Give a bounding box for every malaria parasite, every leukocyte, and every artifact (stain precipitate or debris).
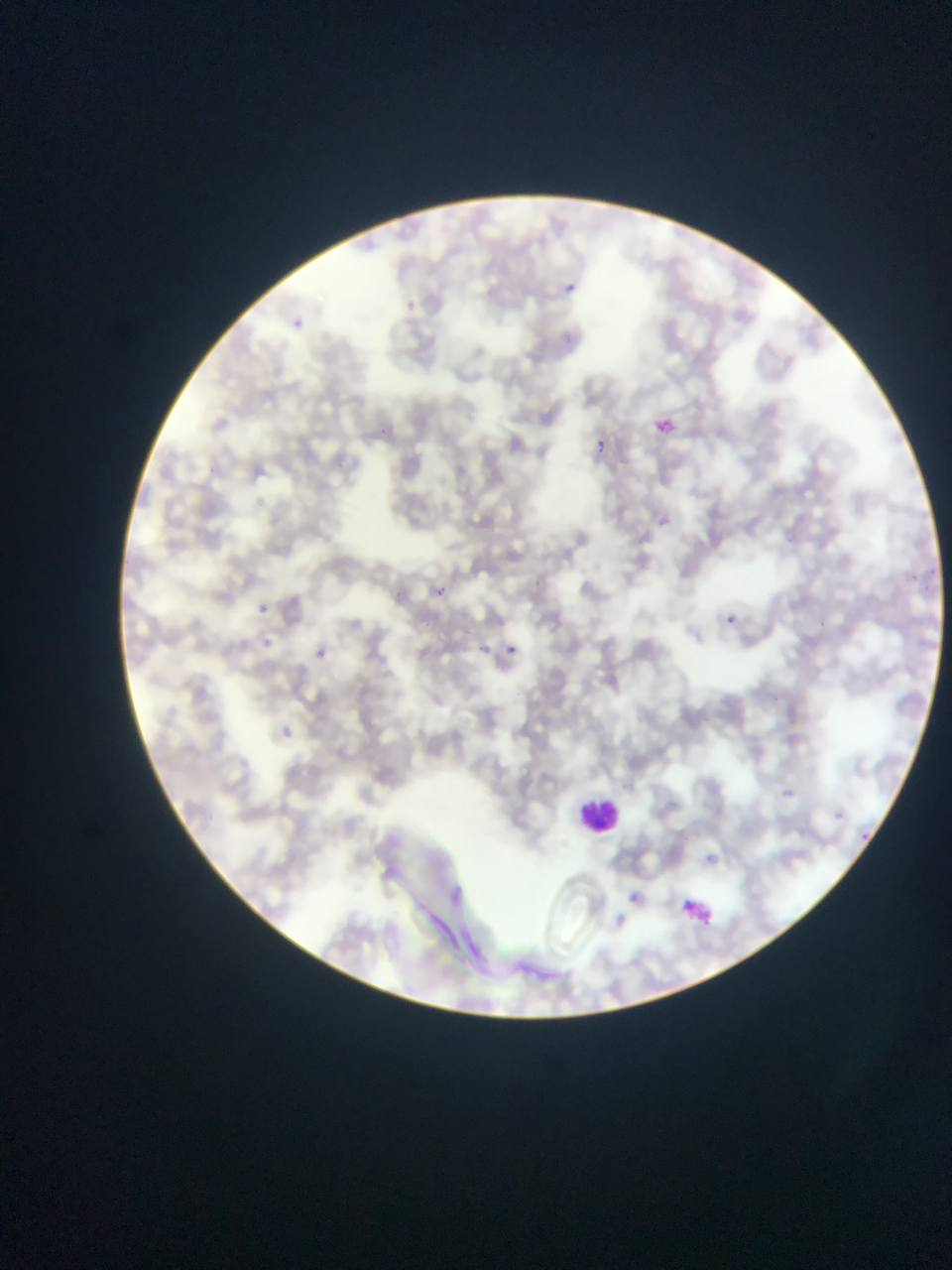

Approximate bounding boxes as {left, top, right, bottom} in pixels.
Malaria parasites: {560, 278, 581, 298}, {402, 279, 435, 317}, {296, 313, 336, 348}, {653, 412, 684, 443}, {598, 435, 629, 468}, {661, 511, 692, 541}, {433, 577, 459, 605}, {258, 592, 286, 618}, {714, 602, 745, 630}, {473, 630, 496, 647}, {504, 632, 524, 653}, {312, 640, 350, 666}, {785, 787, 823, 813}, {702, 848, 737, 869}, {626, 885, 684, 938}, {673, 890, 729, 936}.
Leukocytes: {580, 793, 622, 834}.

capture = mobile-phone photograph through a microscope
preparation = thin blood smear
country = Ghana
image size = 952×1270 pixels
field of view = single